Name the parasite shown.
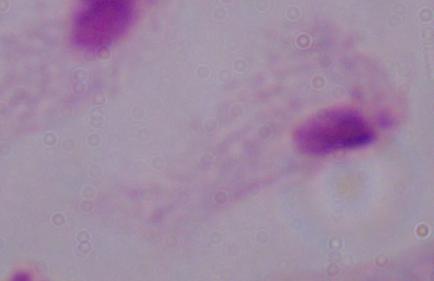
This is a trichomonad.

Summary:
  - Modality: photomicrograph
  - Magnification: 1000x